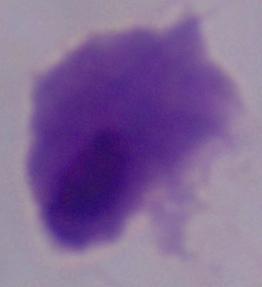

magnification = 1000x
modality = photomicrograph
identification = trichomonad